Classify this cell by malaria status.
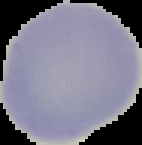
It is uninfected.

Segmented cell region on a black background. From a thin blood film. Image is 142×145 pixels.